Locate every uninfected red blood cell.
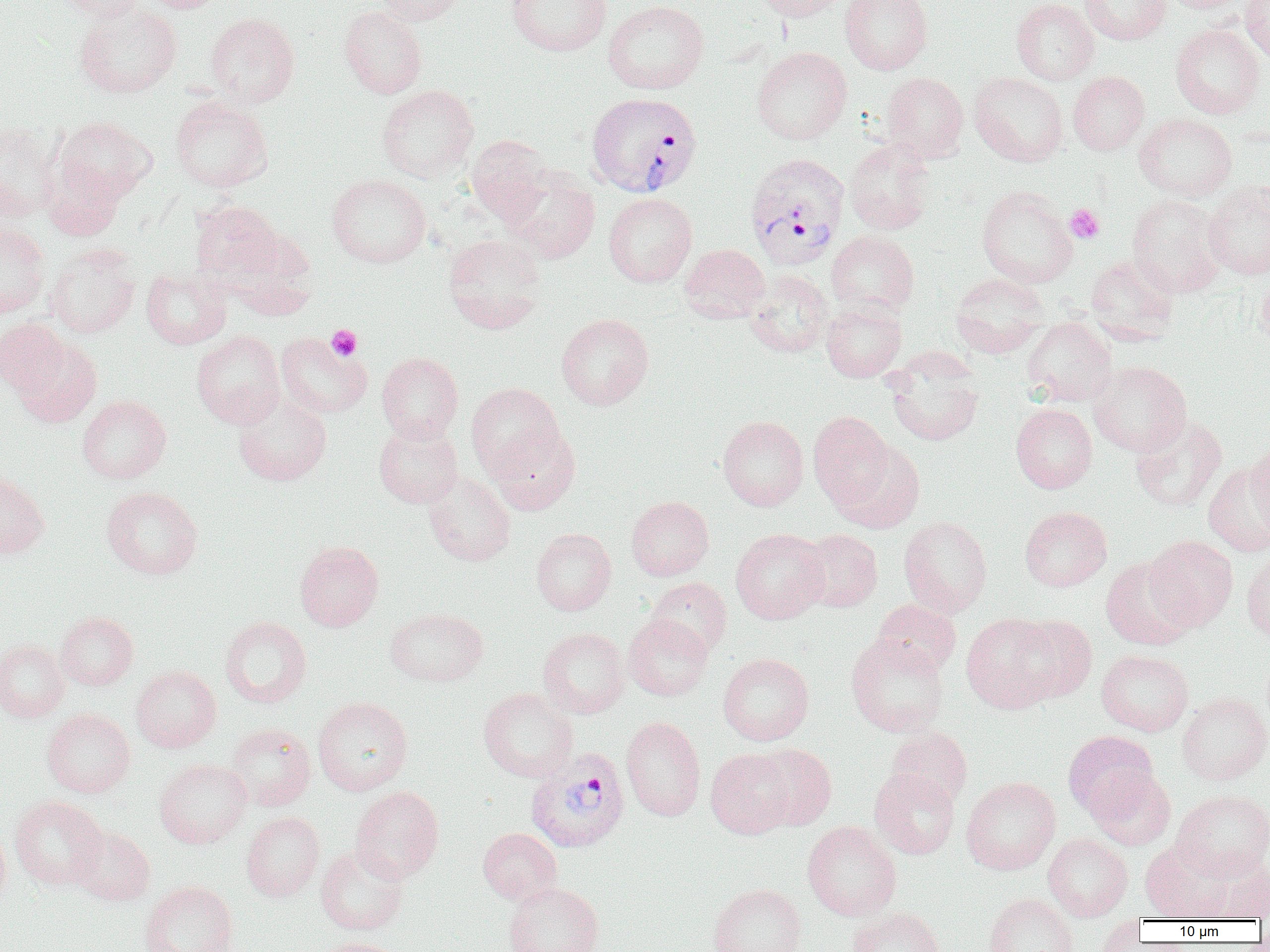
Approximate bounding boxes as (x1, y1, x2, y2) in pixels.
Uninfected red blood cells: (53, 0, 146, 21), (136, 0, 229, 13), (374, 0, 466, 25), (506, 0, 612, 56), (751, 0, 848, 20), (839, 0, 933, 75), (1011, 0, 1099, 84), (1079, 0, 1171, 45), (1160, 0, 1250, 13), (1240, 0, 1270, 65), (603, 1, 709, 94), (73, 2, 182, 99), (338, 5, 427, 99), (204, 13, 299, 107), (1170, 23, 1265, 119), (752, 47, 852, 144), (1068, 71, 1150, 155), (881, 72, 969, 162), (969, 72, 1068, 166), (377, 85, 479, 182), (170, 96, 272, 192), (1134, 113, 1237, 201), (53, 116, 157, 205), (0, 121, 62, 222), (466, 135, 553, 225), (844, 138, 935, 235), (42, 160, 125, 240), (503, 165, 600, 263), (326, 173, 431, 268), (1203, 180, 1270, 279), (976, 185, 1078, 288), (603, 193, 697, 287), (1127, 194, 1226, 296), (190, 201, 283, 285), (0, 220, 50, 318), (826, 231, 919, 317), (443, 234, 546, 334), (46, 244, 140, 338), (679, 244, 770, 323), (1085, 254, 1180, 342), (141, 268, 231, 349), (745, 270, 833, 358), (1256, 270, 1270, 348), (950, 272, 1048, 358), (821, 298, 906, 382), (556, 313, 654, 411), (1022, 317, 1117, 406), (0, 318, 69, 395), (191, 330, 285, 428), (275, 333, 372, 418), (12, 335, 101, 428), (377, 352, 463, 442), (884, 353, 984, 447), (1088, 361, 1192, 457), (466, 383, 564, 478), (233, 394, 331, 486), (77, 395, 171, 483), (1011, 403, 1097, 493), (808, 411, 896, 511), (1130, 415, 1227, 513), (717, 416, 808, 511), (373, 421, 463, 508), (488, 425, 580, 515), (831, 440, 925, 534), (1245, 443, 1270, 540), (1203, 461, 1269, 557), (0, 471, 49, 561), (423, 471, 516, 566), (101, 486, 202, 579), (626, 496, 714, 581), (1019, 506, 1112, 592), (898, 515, 992, 617), (531, 528, 616, 615), (730, 528, 829, 624), (797, 529, 883, 612), (1145, 535, 1238, 630), (295, 541, 384, 631), (1241, 549, 1270, 645), (1100, 556, 1197, 650), (645, 577, 732, 658), (872, 599, 961, 677), (385, 607, 488, 686), (55, 611, 138, 690), (623, 613, 713, 701), (961, 613, 1064, 713), (219, 615, 312, 708), (1010, 615, 1097, 703), (537, 627, 630, 719), (846, 634, 950, 737), (0, 639, 69, 722), (1096, 648, 1194, 736), (718, 652, 814, 745), (131, 665, 221, 752), (478, 687, 578, 782), (1176, 692, 1270, 785), (313, 696, 413, 796), (41, 708, 135, 798), (621, 716, 706, 821), (225, 723, 315, 811), (886, 727, 972, 808), (1063, 730, 1158, 819), (750, 743, 837, 831), (706, 748, 796, 839), (154, 758, 253, 849), (1086, 766, 1176, 850), (869, 767, 960, 860), (961, 776, 1061, 875), (350, 785, 444, 883), (1172, 789, 1270, 880), (10, 795, 107, 890), (241, 811, 325, 901), (802, 821, 901, 921), (0, 823, 11, 913), (70, 826, 154, 906), (477, 827, 562, 904), (1043, 833, 1133, 921), (1141, 840, 1234, 921), (316, 845, 409, 935), (1214, 861, 1270, 920), (139, 881, 238, 952), (503, 881, 603, 952), (708, 883, 806, 952), (984, 893, 1078, 952), (846, 906, 945, 952), (1091, 917, 1148, 952), (316, 937, 406, 952).

Platelet locations: (1065, 204, 1105, 243), (326, 324, 363, 360). Plasmodium vivax-infected red blood cell locations: (586, 91, 702, 198), (745, 153, 850, 270), (526, 749, 631, 853). Slide-level diagnosis: Plasmodium vivax. Optical microscopy. Thin blood smear. Captured at 1000x magnification. Image is 1270×952 pixels. Single field of view.